Point out each Plasmodium parasite.
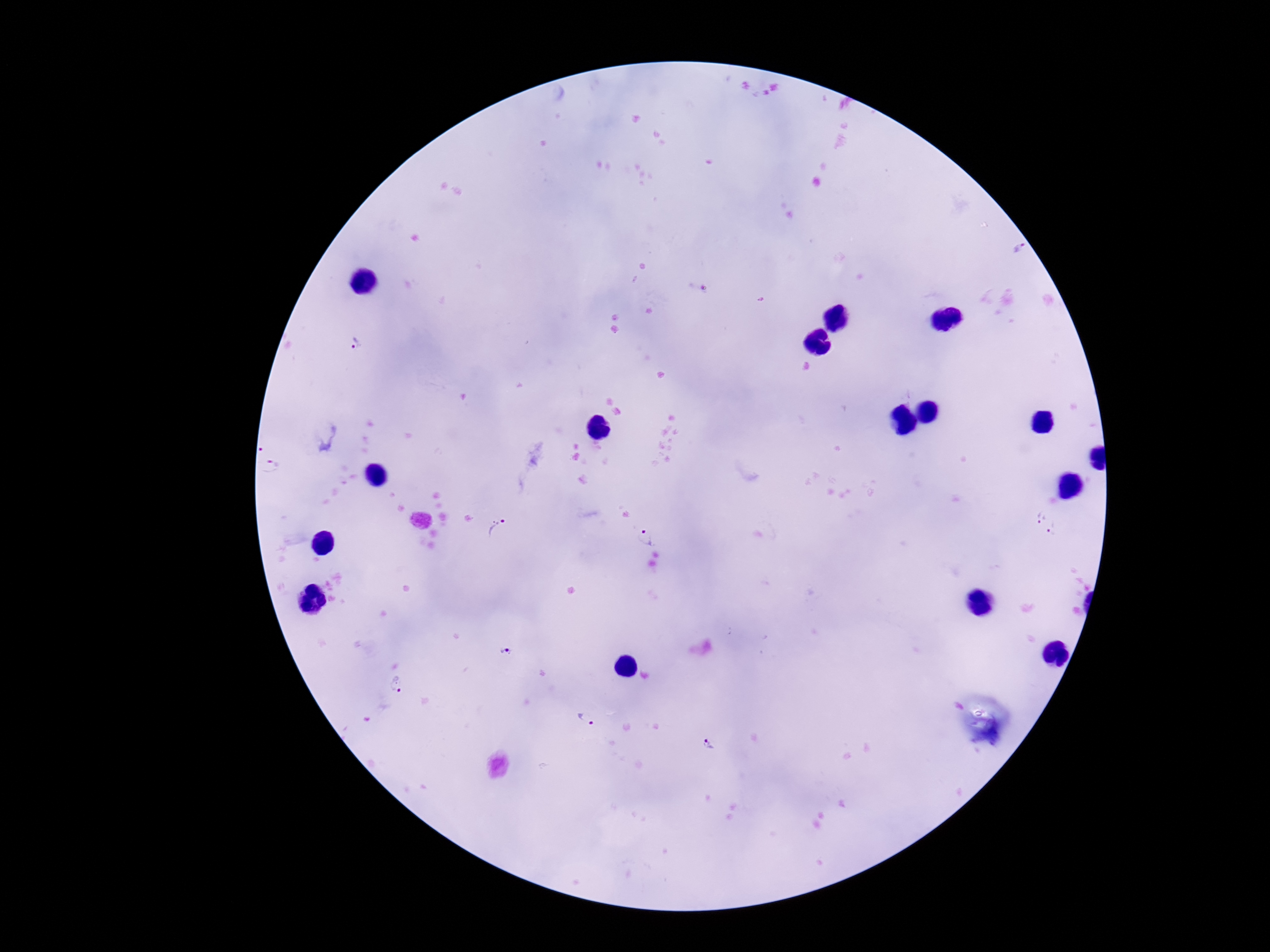
Approximate centers as [x, y] in pixels.
Plasmodium parasites: [355, 344], [1040, 517], [498, 528], [1056, 530], [646, 537], [504, 652], [396, 685], [586, 719], [708, 744].

Summary:
  - Capture: smartphone camera through the microscope eyepiece
  - Stain: Giemsa
  - Patient malaria status: infected
  - Magnification: 100x
  - Image size: 1270×952 pixels
  - Preparation: thick blood smear
  - Field of view: single